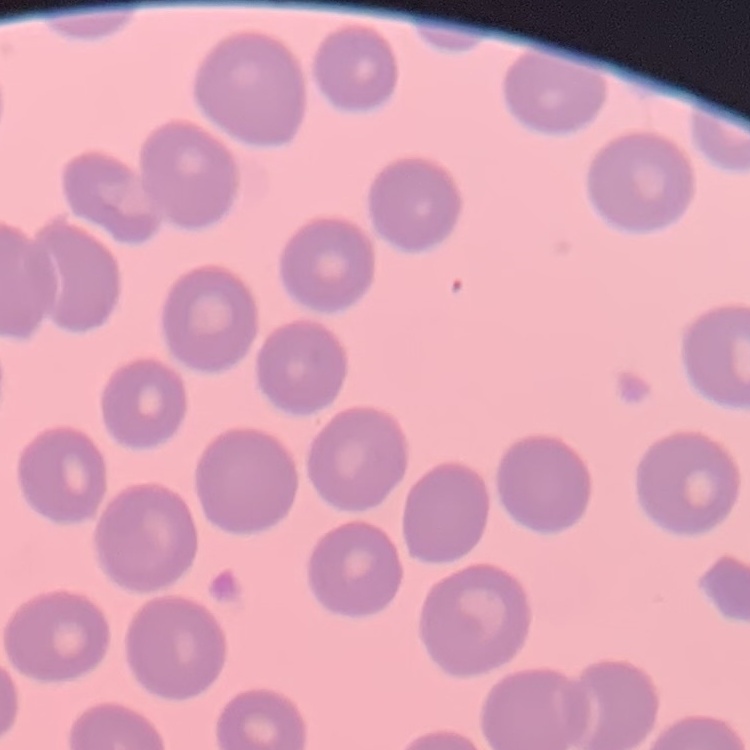
erythrocyte morphology = no rouleaux formation
preparation = thin blood smear
stain = Field's or Giemsa
image type = square crop of a larger photomicrograph